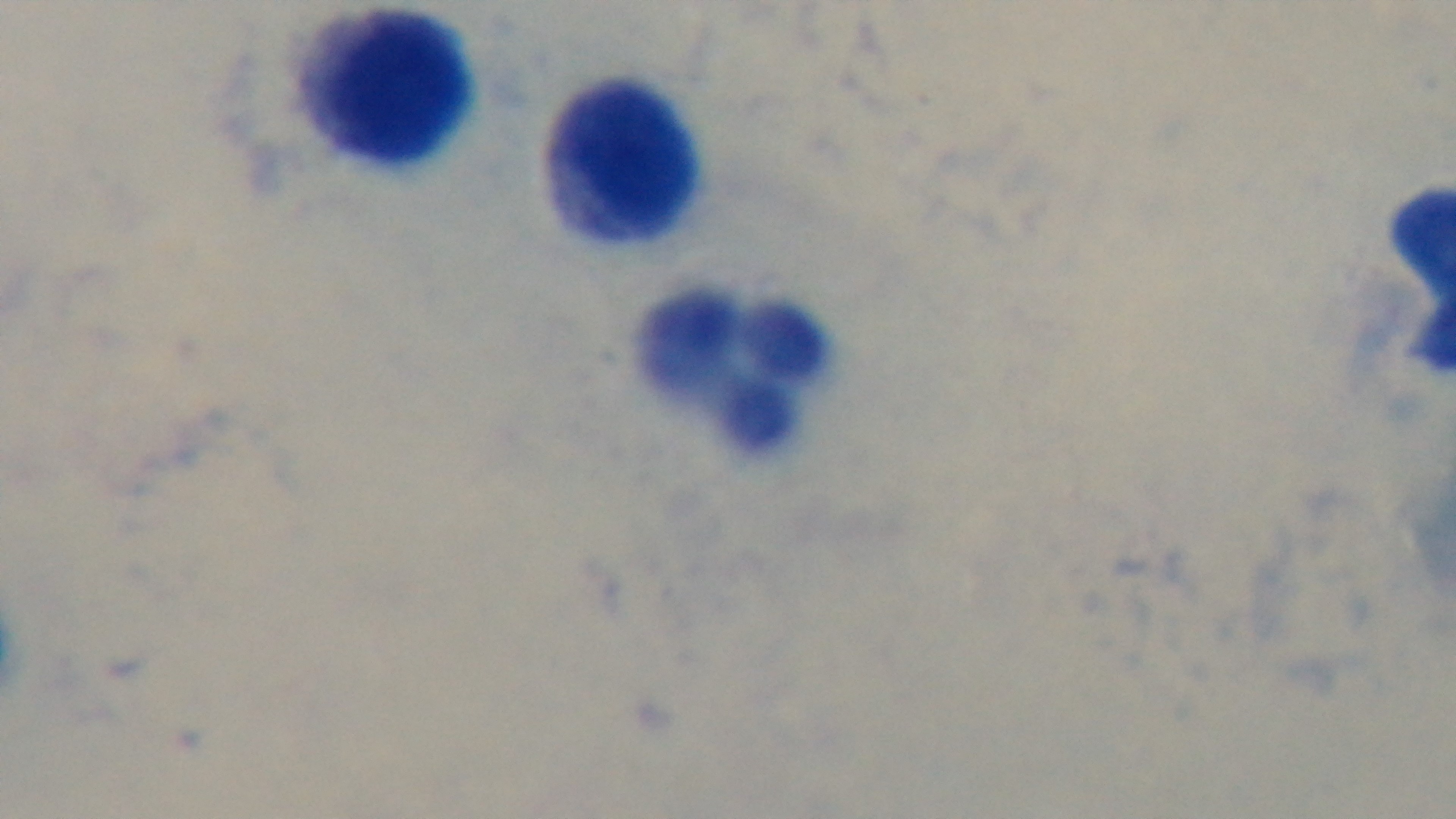
Giemsa-stained. Malaria status: negative. Photomicrograph. Preparation: thick blood film. One field from the slide. Mounted 4K digital camera. 100x oil-immersion objective.